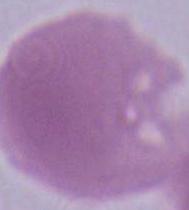
Summary:
  - Identification: erythrocyte
  - Modality: micrograph
  - Magnification: 1000x